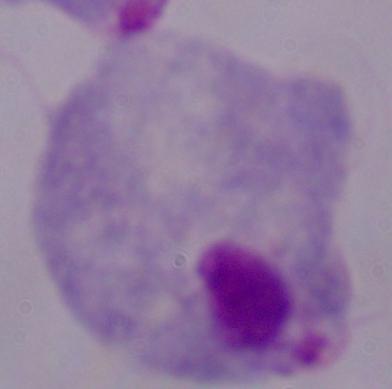
magnification: 1000x
modality: photomicrograph
identification: trichomonad